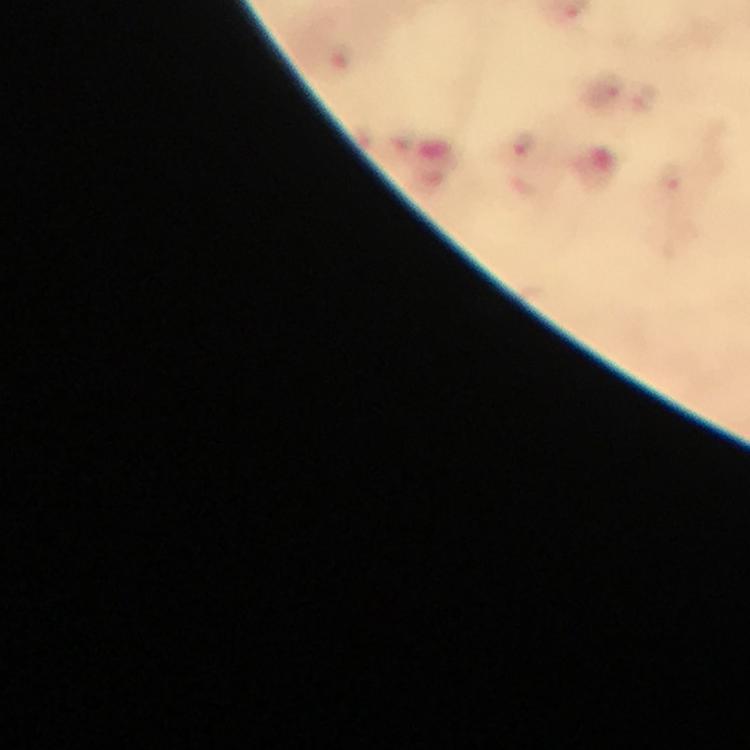
Approximate object centers, in pixels from the top-left corner. Malaria parasite locations: (x=643, y=96), (x=522, y=144). Photographed with a smartphone mounted on the microscope. Giemsa-stained preparation. From a malaria diagnostic workup. Thick blood smear. Immersion oil was used. At 100x magnification. Image is 750×750 pixels. Cropped region of a single field of view.